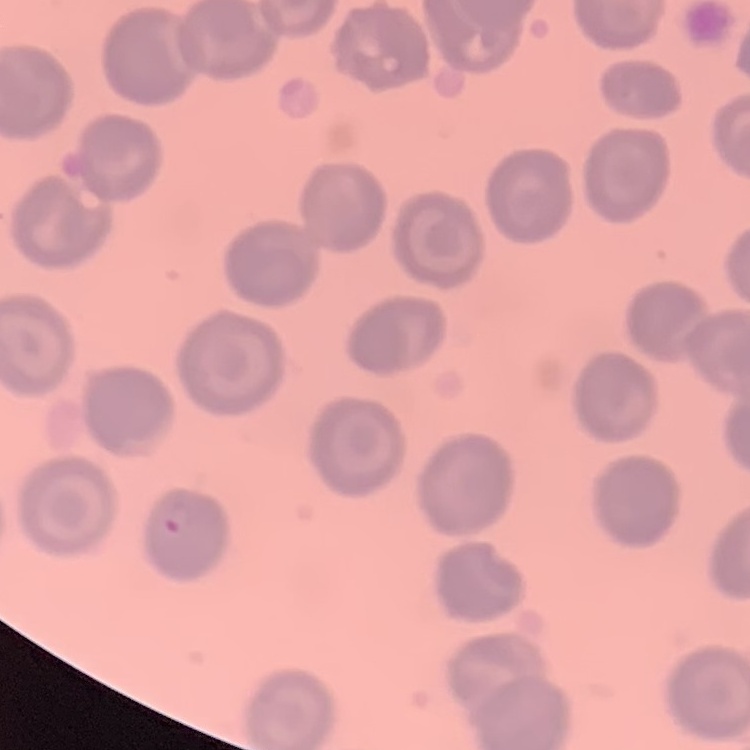

Summary:
  - Erythrocyte morphology: no rouleaux formation
  - Preparation: thin blood film
  - Image type: one tile cut from a larger photomicrograph
  - Stain: Field's or Giemsa